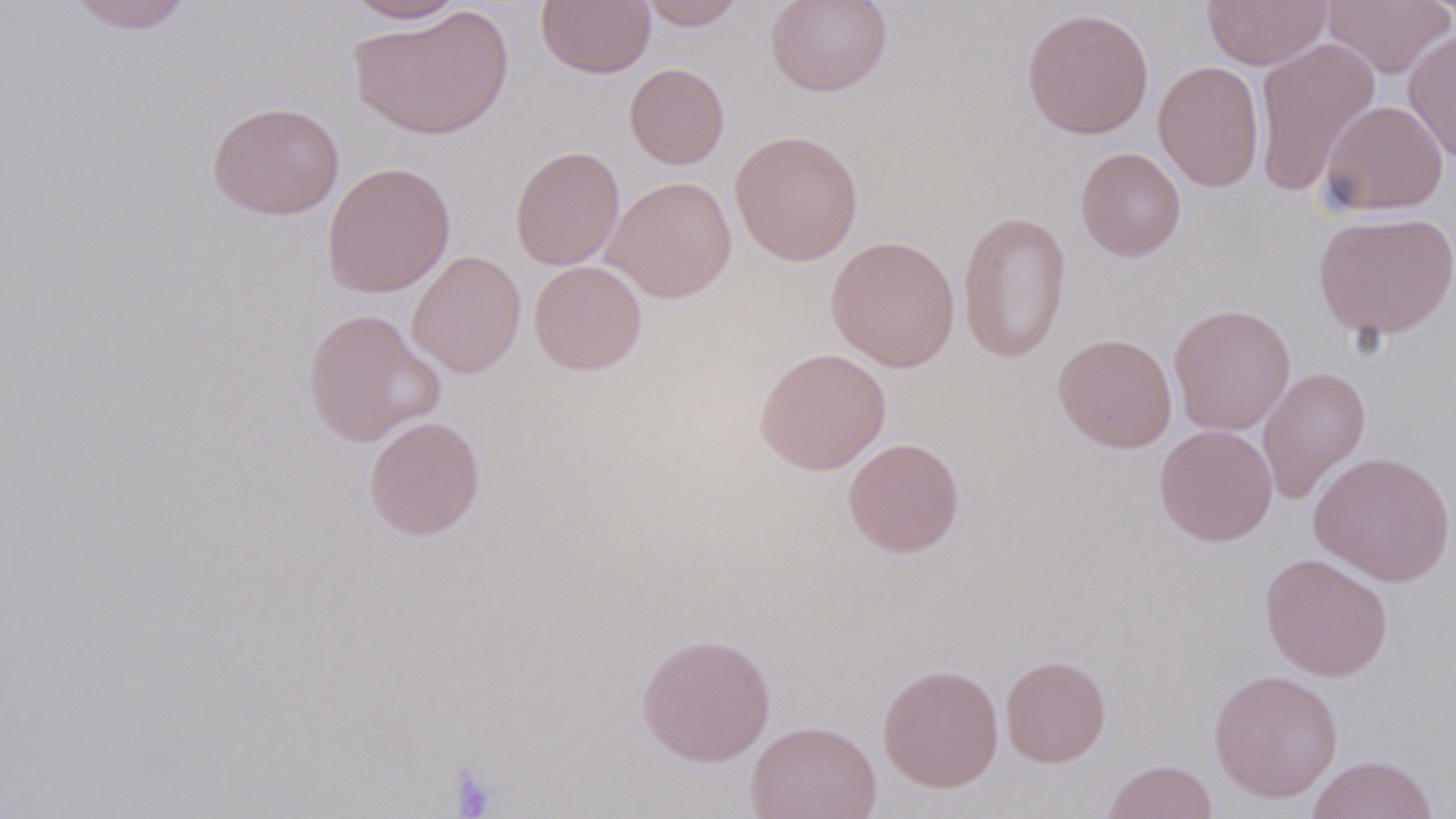

Summary:
  - Coordinate format: approximate bounding boxes as (x1, y1, x2, y2) in pixels
  - Uninfected red blood cell locations: (65, 0, 195, 34), (342, 0, 469, 24), (637, 0, 748, 30), (765, 0, 893, 97), (1201, 0, 1332, 70), (1321, 0, 1456, 78), (537, 1, 656, 78), (348, 7, 514, 141), (1021, 7, 1154, 139), (1403, 29, 1456, 165), (1252, 37, 1381, 196), (1153, 61, 1265, 192), (625, 63, 729, 169), (1319, 100, 1449, 216), (207, 101, 344, 220), (730, 129, 864, 266), (510, 145, 625, 271), (1075, 147, 1186, 262), (321, 161, 455, 299), (603, 175, 738, 303), (957, 210, 1072, 364), (1312, 211, 1456, 340), (826, 235, 960, 372), (407, 250, 526, 378), (528, 260, 647, 375), (1169, 303, 1296, 435), (301, 307, 445, 448), (1052, 333, 1178, 453), (754, 347, 892, 475), (1258, 366, 1371, 505), (364, 415, 485, 541), (1153, 424, 1278, 547), (842, 437, 965, 558), (1308, 450, 1455, 586), (1260, 552, 1394, 681), (636, 631, 776, 766), (1000, 655, 1111, 767), (877, 663, 1004, 793), (1209, 669, 1343, 802), (746, 720, 882, 819), (1306, 754, 1438, 819), (1101, 759, 1218, 819)
  - Platelet locations: (447, 764, 500, 818)
  - Slide-level diagnosis: no evidence of blood parasites
  - Magnification: 1000x
  - Image size: 1456×819 pixels
  - Modality: optical microscopy
  - Preparation: thin blood film
  - Stain: May-Grünwald-Giemsa
  - Field of view: single